Classify this cell by malaria status.
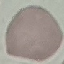
Uninfected.

Summary:
  - Image type: cell patch, automatically extracted from a larger field of view and resized to 64 × 64 pixels
  - Capture: smartphone camera at the microscope eyepiece
  - Stain: Giemsa
  - Preparation: thin smear